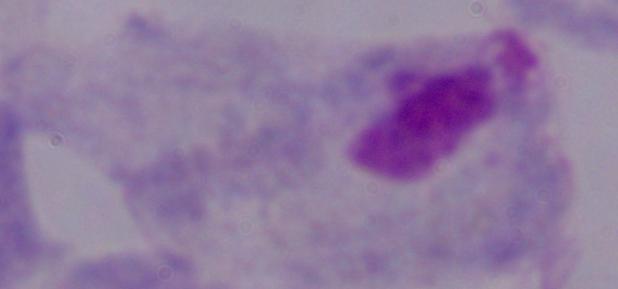
{
  "identification": "trichomonad",
  "magnification": "1000x",
  "modality": "photomicrograph"
}